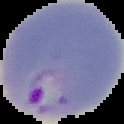

Summary:
  - Preparation: thin blood film
  - Image size: 124×124 pixels
  - Image type: cell region segmented out of the field of view; surrounding area masked to black
  - Malaria status: parasitized